Give the location of every parasitized red blood cell.
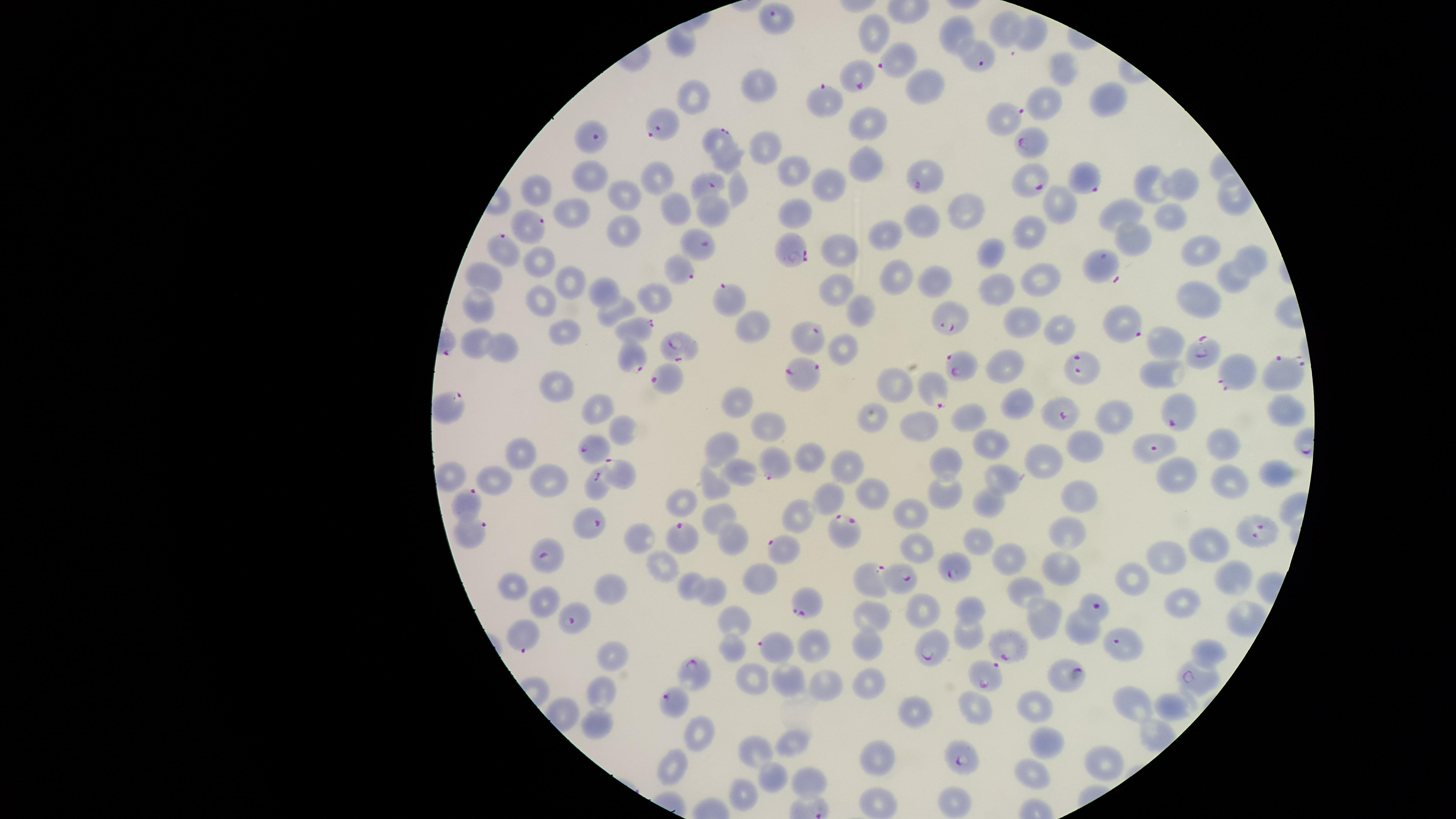

Approximate marker points as (x, y) in pixels.
Parasitized red blood cells: (774, 19), (896, 58), (984, 60), (853, 78), (829, 95), (664, 123), (1004, 123), (717, 133), (594, 136), (1034, 142), (1087, 178), (1029, 180), (708, 181), (921, 183), (527, 226), (501, 243), (696, 243), (795, 249), (1100, 268), (680, 270), (733, 295), (954, 316), (1127, 323), (640, 325), (808, 336), (680, 345), (1198, 351), (634, 356), (1084, 364), (968, 368), (801, 371), (1231, 371), (1274, 371), (662, 375), (938, 391), (1179, 415), (1059, 417), (593, 449), (1154, 451), (777, 464), (617, 476), (595, 487), (463, 502), (593, 524), (848, 530), (1257, 531), (469, 534), (686, 536), (784, 548), (548, 558), (952, 568), (868, 577), (906, 577), (1094, 606), (810, 607), (576, 618), (525, 632), (1121, 643), (932, 647), (776, 648), (1011, 652), (689, 674), (1064, 676), (978, 677), (1198, 683), (673, 700), (964, 757).

Approximate marker points as (x, y) in pixels. Uninfected red blood cells: (1004, 29), (874, 31), (1034, 33), (959, 34), (680, 41), (1060, 68), (918, 84), (758, 85), (698, 95), (1107, 97), (1047, 100), (868, 120), (768, 143), (729, 160), (863, 163), (789, 169), (584, 178), (657, 180), (1152, 184), (1181, 184), (827, 185), (533, 187), (737, 191), (627, 197), (1058, 205), (676, 208), (1119, 211), (574, 212), (794, 212), (965, 213), (1165, 215), (927, 218), (622, 232), (1031, 233), (888, 235), (1126, 240), (1201, 248), (841, 249), (993, 250), (1241, 257), (534, 265), (896, 275), (482, 277), (1043, 279), (1230, 282), (566, 283), (936, 283), (837, 288), (607, 291), (653, 293), (995, 296), (540, 298), (1200, 299), (482, 310), (616, 311), (860, 314), (1016, 322), (752, 327), (1060, 330), (568, 333), (1165, 340), (473, 345), (503, 346), (841, 350), (1008, 365), (1159, 377), (889, 386), (557, 387), (1016, 401), (742, 404), (447, 405), (592, 407), (1286, 410), (1116, 414), (868, 416), (965, 418), (773, 424), (914, 425), (624, 428), (992, 442), (1084, 444), (1219, 448), (722, 449), (514, 454), (946, 462), (1047, 462), (811, 464), (846, 467), (739, 474), (1187, 474), (1272, 474), (541, 475), (450, 478), (494, 478), (1001, 482), (1230, 483), (713, 486), (1075, 490), (877, 494), (944, 496), (830, 499), (994, 505), (680, 509), (914, 515), (721, 518), (794, 518), (982, 536), (1068, 537), (637, 543), (731, 543), (1211, 547), (917, 550), (1014, 559), (1169, 563), (1064, 567), (664, 571), (1133, 581), (1234, 581), (757, 584), (686, 587), (610, 588), (513, 590), (709, 590), (1025, 591), (544, 600), (1185, 603), (968, 611), (927, 612), (738, 617), (874, 619), (1039, 620), (966, 633), (1077, 633), (867, 648), (1208, 649), (732, 650), (615, 655), (750, 680), (783, 682), (866, 684), (823, 688), (603, 692), (968, 700), (1133, 700), (1037, 705), (1169, 708), (910, 714), (599, 723), (701, 735), (795, 740), (1047, 747), (757, 756), (882, 756), (1100, 763), (673, 765), (1034, 778), (810, 779), (781, 785), (745, 797), (950, 802), (882, 805). Smartphone photograph through the microscope eyepiece. Species: Plasmodium falciparum. Circular visible region. One field of view of the specimen. Giemsa-stained preparation. Image is 1456×819 pixels. Thin smear of blood.